Assess for Plasmodium parasites.
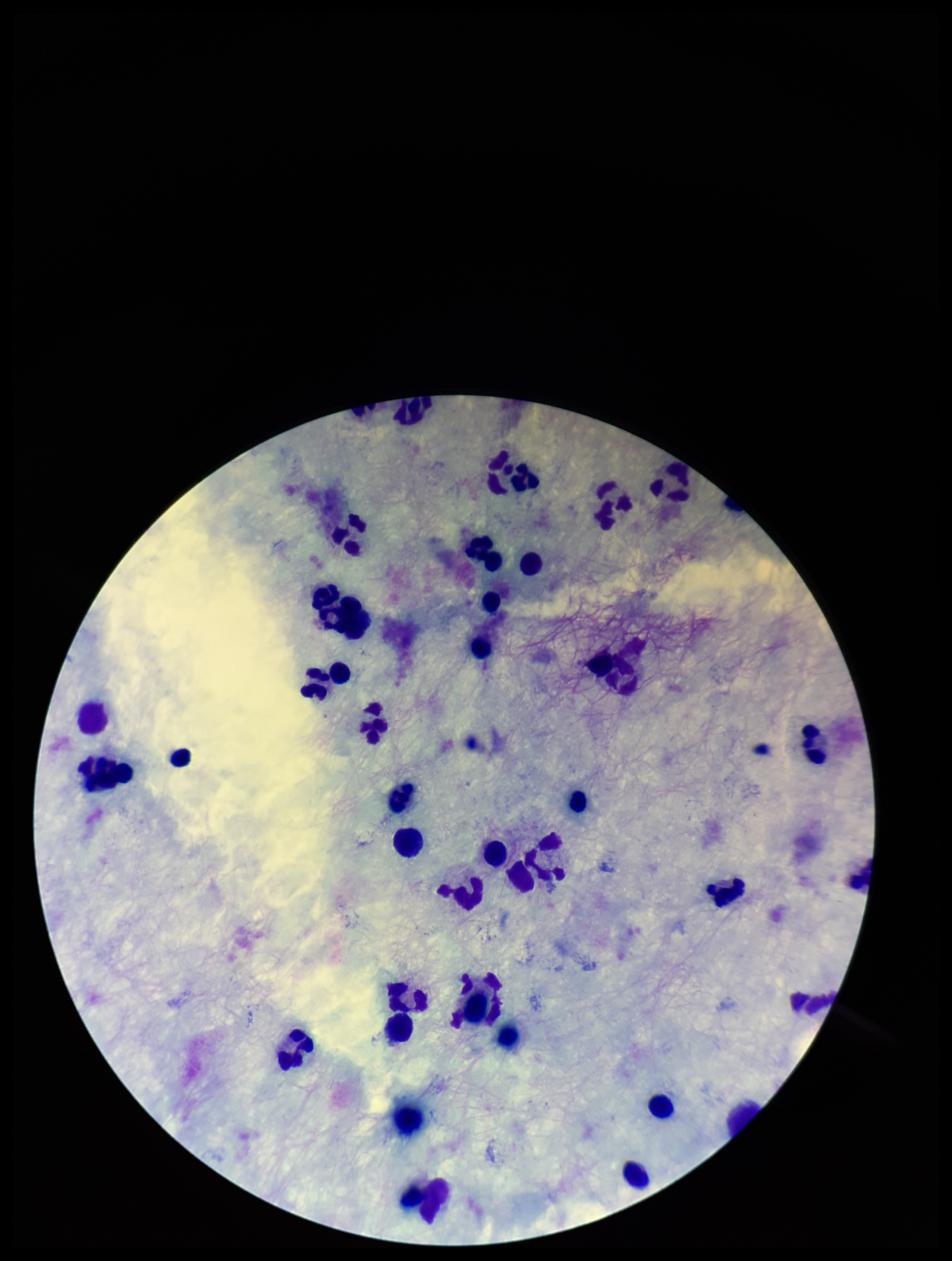
None detected.

Summary:
  - Parasite count: 0
  - Image size: 952×1261 pixels
  - Stain: Giemsa
  - Preparation: thick
  - Field of view: single
  - Capture: smartphone photograph through the microscope eyepiece
  - Leukocyte count: 38
  - Patient malaria status: negative